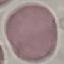

Summary:
  - Malaria status: uninfected
  - Stain: Giemsa
  - Preparation: thin smear
  - Capture: smartphone camera at the microscope eyepiece
  - Image type: cell patch, automatically extracted from a larger field of view and resized to 64 × 64 pixels